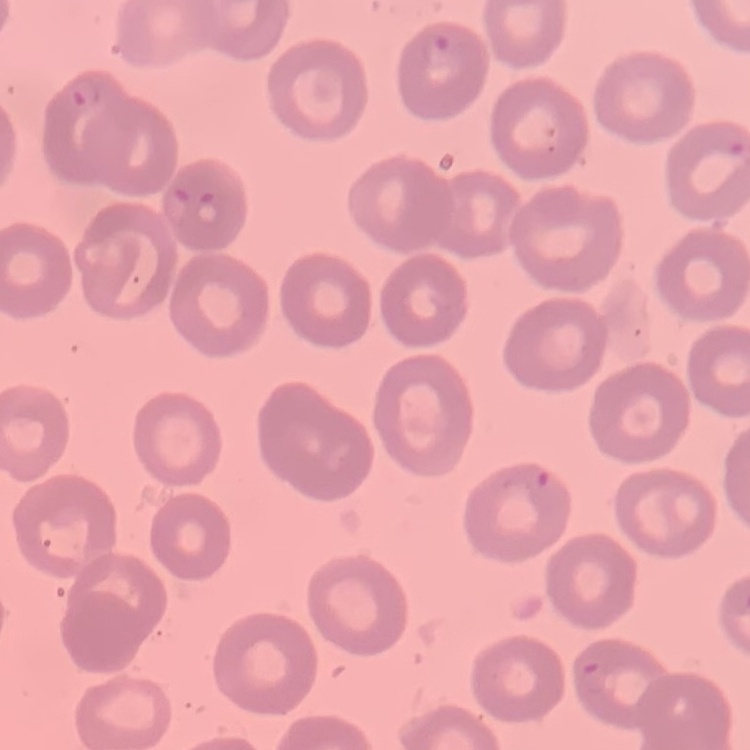
Summary:
  - Erythrocyte morphology: no rouleaux formation
  - Stain: Field's or Giemsa
  - Image type: square crop of a larger photomicrograph
  - Preparation: thin blood smear